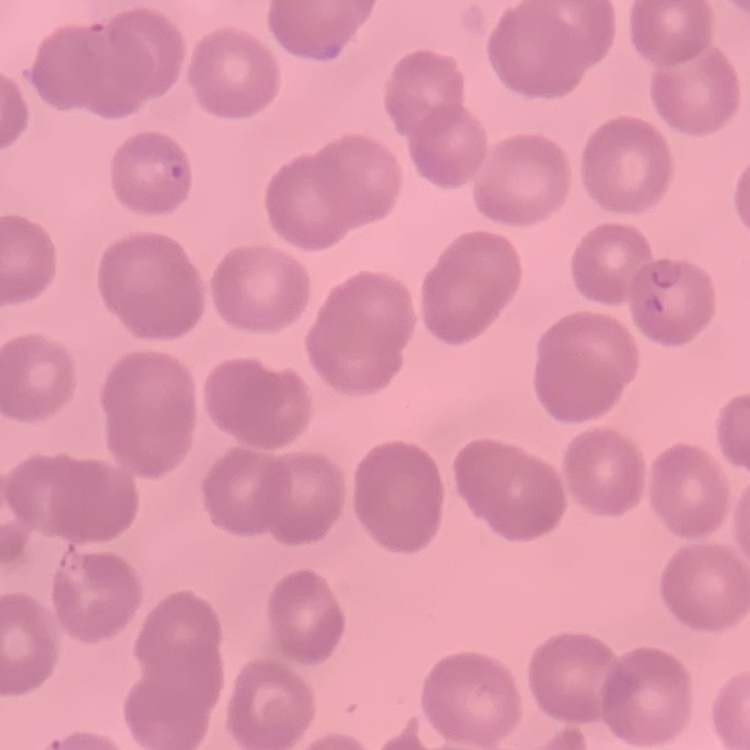

Summary:
  - Red blood cell morphology: no rouleaux formation
  - Stain: Field's or Giemsa
  - Image type: one tile cut from a larger photomicrograph
  - Preparation: thin blood smear